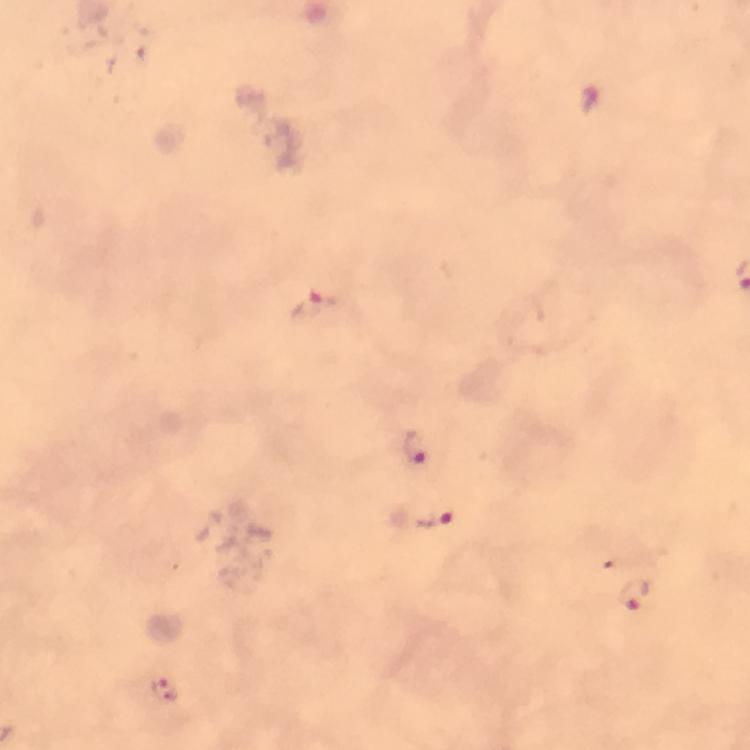

Approximate centers as {x, y} in pixels.
Summary:
  - Plasmodium parasite locations: {315, 306}, {416, 449}, {433, 518}, {631, 594}, {164, 690}
  - Cropped from: a single field of view
  - Stain: Giemsa
  - Capture: smartphone camera through the microscope
  - Immersion oil: used
  - Context: from a diagnostic examination for malaria
  - Magnification: 100x
  - Image size: 750×750 pixels
  - Preparation: thick blood film